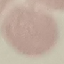

result = no malaria parasites seen
capture = smartphone camera at the microscope eyepiece
image type = automatically extracted cell patch, resized to 64 × 64 pixels
preparation = thin blood film
stain = Giemsa